Classify this cell by malaria status.
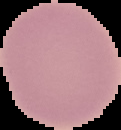

Uninfected.

From a thin blood film. Segmented cell region on a black background. Image is 121×130 pixels.